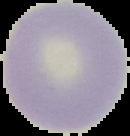

Malaria status: uninfected. Segmented cell region on a black background. Image is 130×136 pixels. From a thin blood film.